Identify the parasite.
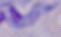

This is a trypanosome.

Photomicrograph. 1000x magnification.